State which cell type is depicted.
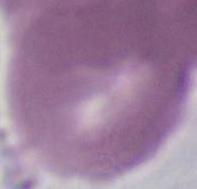

This is an erythrocyte.

Micrograph. 1000x magnification.